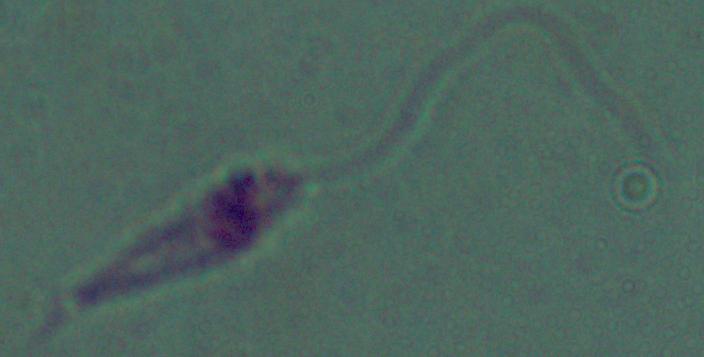 Photomicrograph. A Leishmania parasite is shown. Captured at 1000x magnification.